Classify this cell by malaria status.
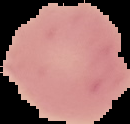

It is uninfected.

From a thin blood smear. Segmented cell region on a black background. Image is 130×124 pixels.